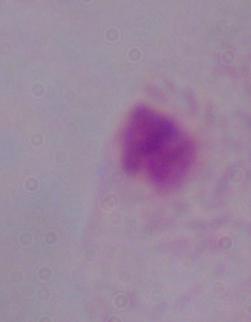

magnification = 1000x
identification = trichomonad
modality = micrograph